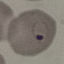
Summary:
  - Malaria status: parasitized
  - Stain: Giemsa
  - Image type: cell patch, automatically extracted from a larger field of view and resized to 64 × 64 pixels
  - Preparation: thin blood smear
  - Capture: smartphone through the microscope eyepiece